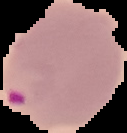 The area outside the segmented cell region is set to black. Malaria status: parasitized. Image is 127×133 pixels. From a thin blood film.